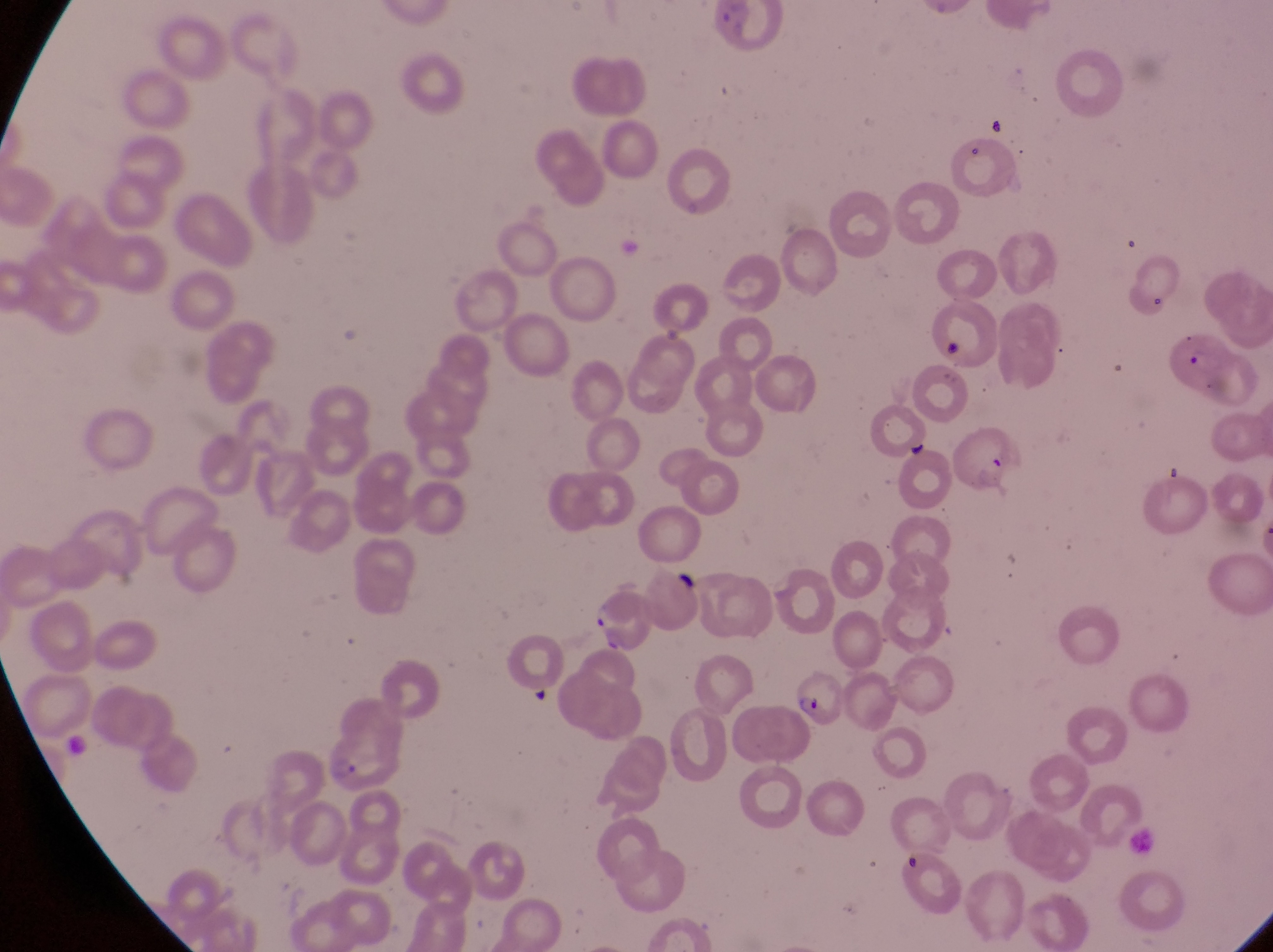 Approximate bounding boxes as [left, top, right, bottom] in pixels. Artifact (platelet-like body, stain precipitate, or debris) locations: [896, 849, 929, 874]. Parasitised red blood cell locations: [1168, 325, 1260, 408], [949, 424, 1021, 498], [582, 594, 659, 654], [794, 675, 841, 732], [319, 729, 397, 791]. Thin blood smear. Photographed through the eyepiece of an Olympus CX-23 microscope with a smartphone camera. Image is 1273×952 pixels. Single field of view. Collected in Uganda. Magnification of 1000x.